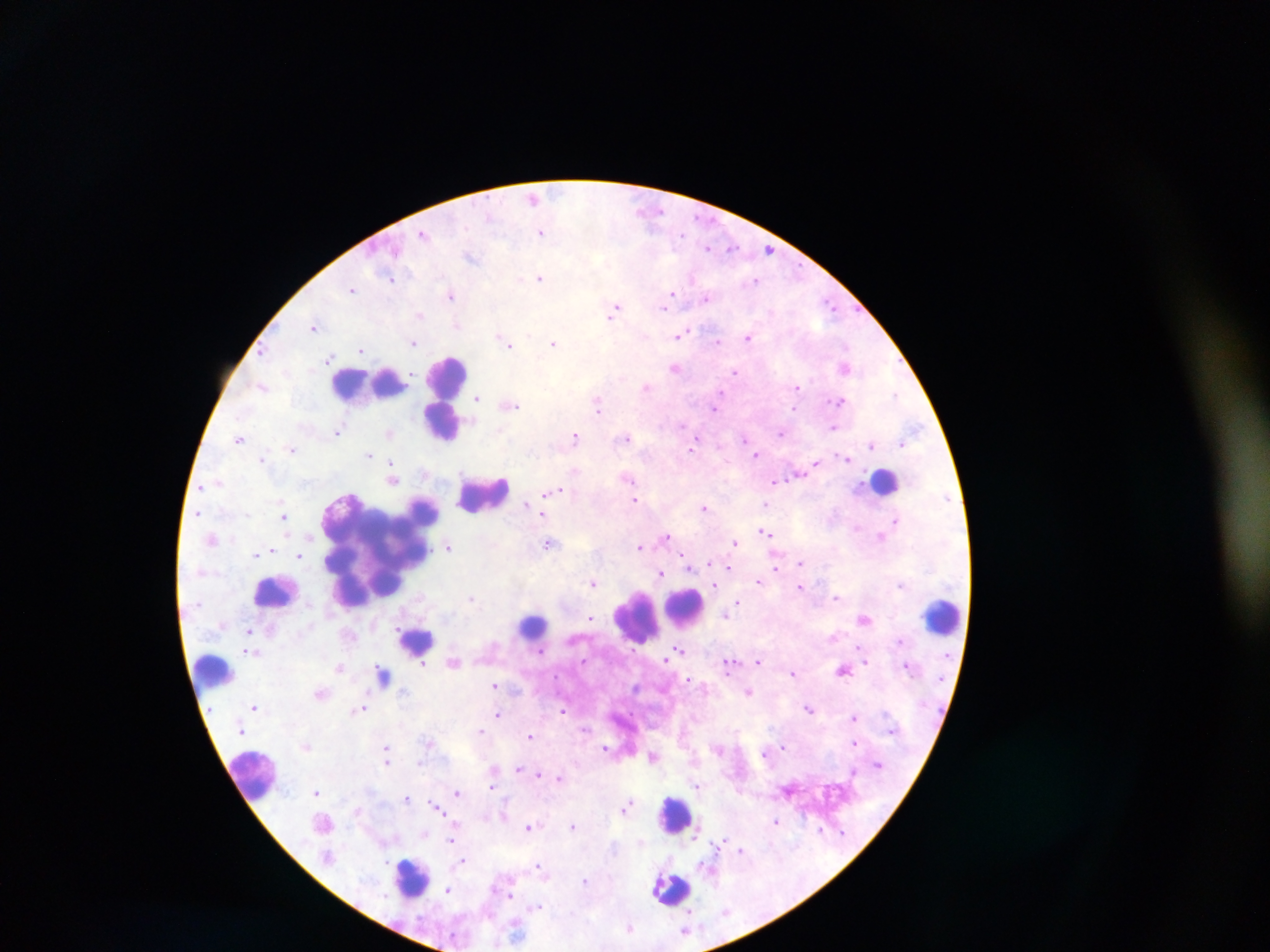

leukocyte locations = approximate centers as x y in pixels: 449 373; 367 388; 442 421; 883 485; 485 494; 379 547; 280 591; 692 612; 942 617; 533 620; 639 620; 417 641; 210 670; 255 768; 674 810; 405 873; 667 886
field of view = single
malaria parasite locations = approximate centers as x y in pixels: 532 197; 640 207; 489 217; 464 227; 543 233; 424 234; 682 235; 732 246; 708 248; 768 249; 395 251; 471 258; 390 278; 540 279; 756 281; 692 283; 353 289; 450 295; 708 298; 667 301; 830 305; 615 307; 419 315; 611 316; 456 324; 312 327; 680 336; 749 337; 500 338; 719 341; 414 343; 554 344; 264 349; 361 350; 329 356; 847 366; 674 368; 411 372; 735 372; 261 385; 646 386; 797 387; 895 394; 477 400; 840 400; 599 401; 517 407; 796 407; 509 408; 714 409; 599 411; 683 424; 833 428; 338 432; 390 432; 782 432; 576 435; 240 438; 627 438; 744 438; 902 443; 871 445; 295 448; 691 450; 530 454; 369 455; 757 456; 847 457; 262 458; 815 463; 390 470; 797 475; 218 481; 774 481; 201 486; 551 493; 355 494; 636 500; 766 504; 527 505; 704 508; 198 511; 543 514; 284 517; 895 520; 764 532; 667 535; 307 538; 881 538; 549 543; 734 543; 449 546; 639 547; 275 551; 258 554; 299 557; 800 562; 691 568; 728 568; 776 568; 660 574; 593 582; 757 583; 716 585; 900 585; 801 588; 471 597; 836 597; 738 604; 725 615; 591 617; 242 632; 860 645; 678 647; 542 651; 583 660; 666 660; 758 662; 423 663; 867 663; 729 664; 338 668; 845 671; 792 673; 383 676; 689 679; 495 685; 750 692; 258 709; 359 709; 809 710; 563 711; 497 716; 854 719; 481 731; 529 735; 854 742; 386 747; 607 747; 783 747; 306 748; 765 753; 420 763; 386 764; 520 765; 517 770; 853 771; 539 773; 561 778; 698 786; 492 788; 316 791; 457 793; 406 798; 627 806; 437 807; 442 815; 775 821; 528 827; 573 827; 819 829; 695 833; 641 840; 720 840; 451 841; 741 850; 462 861; 384 862; 537 864; 584 880; 448 889; 509 894; 539 906; 690 907; 686 931
capture = mobile-phone photograph through a microscope
country = Ghana
preparation = thick blood smear
image size = 1270×952 pixels